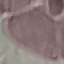
Summary:
  - Malaria status: uninfected
  - Capture: smartphone camera at the microscope eyepiece
  - Stain: Giemsa
  - Preparation: thin smear
  - Image type: cell patch, automatically extracted from a larger field of view and resized to 64 × 64 pixels